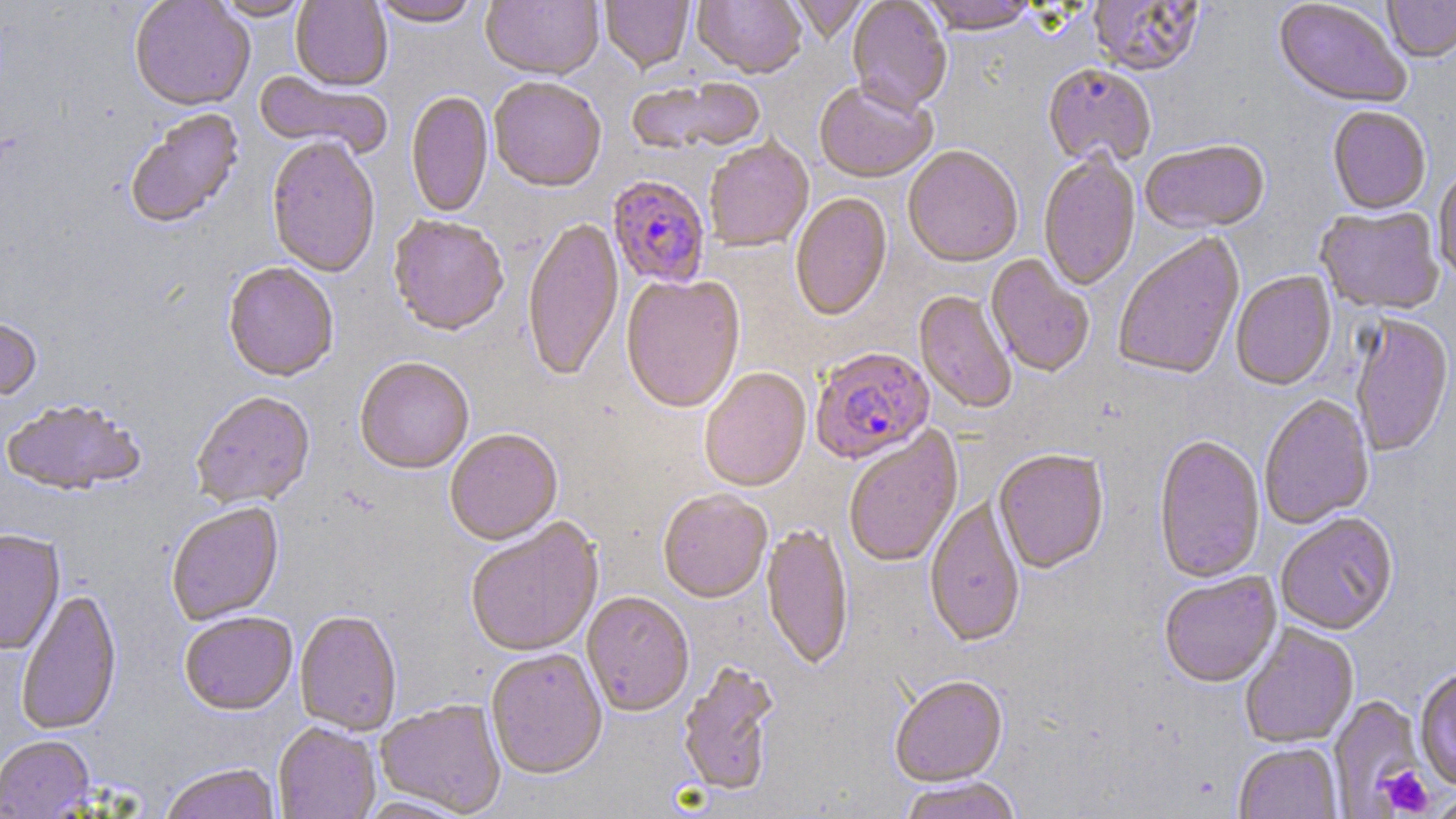

Summary:
  - Coordinate format: approximate bounding boxes as (x1, y1, x2, y2) in pixels
  - Uninfected red blood cell locations: (129, 0, 255, 114), (213, 0, 311, 22), (290, 0, 392, 93), (371, 0, 482, 29), (481, 0, 604, 83), (600, 0, 694, 75), (693, 0, 806, 81), (790, 0, 870, 44), (846, 0, 952, 117), (921, 0, 1041, 38), (1088, 0, 1205, 77), (1383, 0, 1456, 65), (1273, 1, 1411, 110), (1042, 65, 1156, 171), (253, 70, 392, 162), (626, 79, 767, 158), (488, 80, 606, 195), (813, 83, 937, 185), (406, 92, 493, 220), (1327, 108, 1431, 216), (125, 109, 244, 231), (266, 138, 380, 280), (704, 140, 814, 253), (1140, 141, 1270, 237), (903, 148, 1023, 270), (1038, 153, 1140, 293), (1433, 168, 1456, 286), (790, 193, 893, 323), (1315, 207, 1445, 317), (388, 218, 508, 338), (523, 219, 624, 384), (1112, 234, 1246, 383), (985, 255, 1095, 379), (223, 263, 339, 384), (1230, 272, 1338, 392), (621, 277, 746, 415), (914, 291, 1016, 415), (1349, 317, 1455, 459), (0, 318, 42, 404), (354, 360, 473, 477), (699, 369, 812, 494), (191, 394, 315, 510), (1259, 395, 1375, 531), (1, 402, 146, 498), (844, 427, 964, 569), (445, 431, 563, 548), (1153, 436, 1265, 585), (993, 452, 1109, 576), (658, 492, 772, 605), (924, 499, 1025, 650), (167, 505, 285, 627), (1276, 514, 1399, 636), (465, 520, 604, 659), (761, 525, 853, 672), (0, 531, 65, 657), (1159, 572, 1281, 689), (16, 591, 122, 737), (582, 593, 694, 718), (295, 612, 403, 736), (179, 613, 297, 717), (1239, 624, 1359, 749), (486, 650, 607, 781), (677, 661, 780, 799), (1414, 667, 1456, 791), (890, 678, 1009, 790), (1327, 695, 1426, 815), (375, 700, 506, 816), (273, 723, 381, 819), (0, 736, 96, 818), (1233, 744, 1343, 819), (160, 764, 281, 819), (899, 778, 1024, 819), (1430, 791, 1456, 819)
  - Platelet locations: (1377, 765, 1434, 817), (1428, 791, 1456, 818)
  - Plasmodium falciparum-infected red blood cell locations: (608, 176, 710, 290), (811, 348, 935, 465)
  - Slide-level diagnosis: Plasmodium falciparum
  - Image size: 1456×819 pixels
  - Magnification: 1000x
  - Modality: optical microscopy
  - Field of view: one of a larger specimen
  - Preparation: thin blood film
  - Stain: May-Grünwald-Giemsa